Identify the blood parasite species.
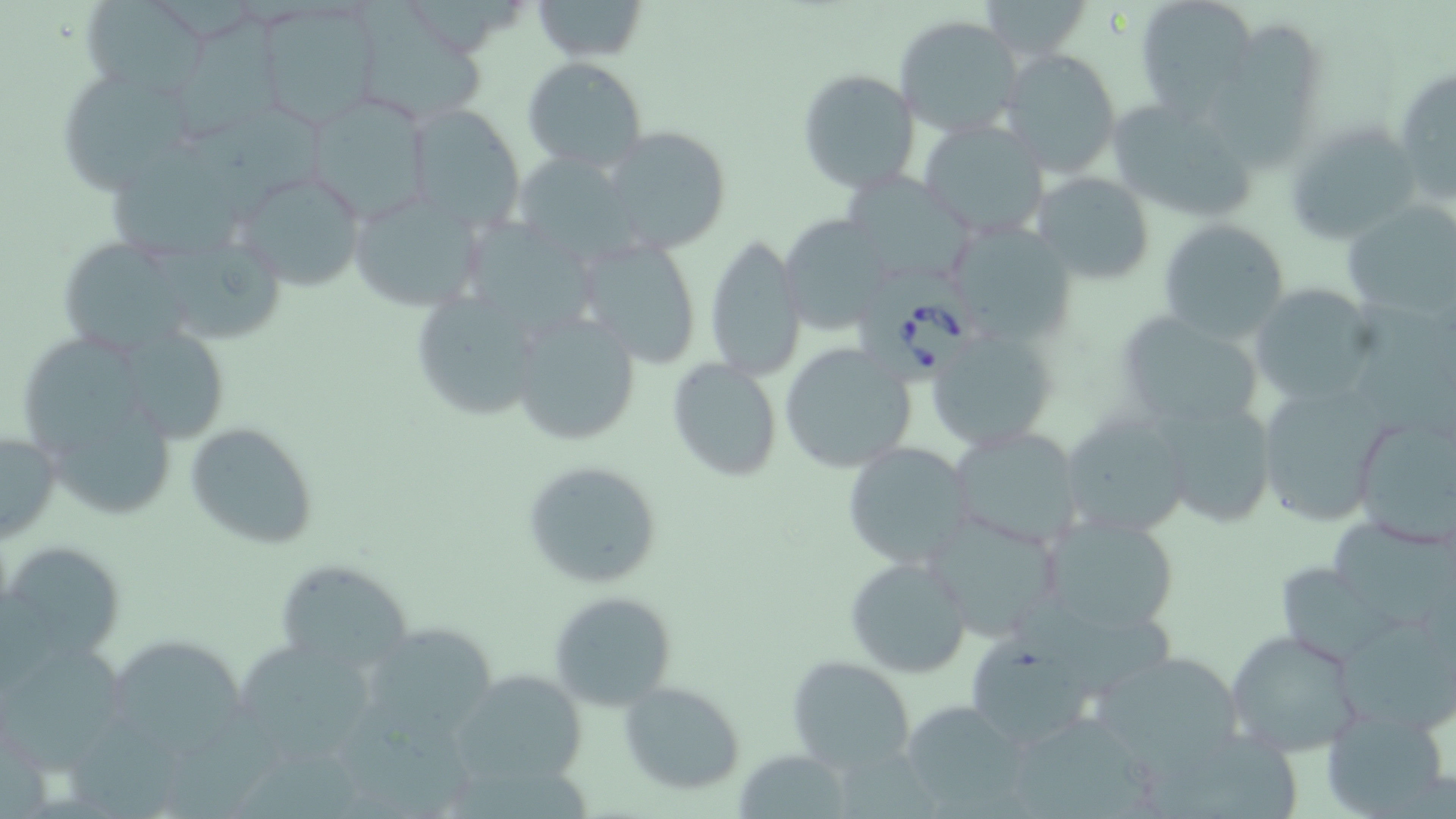

Babesia divergens.

image_size: 1456×819 pixels
preparation: thin blood smear
modality: optical microscopy
uninfected_red_blood_cell_locations: 'approximate bounding boxes as named x1/y1/x2/y2 corners in pixels: (x1=79, y1=0, x2=213, y2=99), (x1=529, y1=0, x2=649, y2=63), (x1=982, y1=0, x2=1094, y2=62), (x1=1133, y1=0, x2=1257, y2=111), (x1=254, y1=3, x2=381, y2=129), (x1=363, y1=4, x2=483, y2=126), (x1=173, y1=14, x2=291, y2=144), (x1=894, y1=14, x2=1026, y2=137), (x1=999, y1=48, x2=1123, y2=178), (x1=522, y1=56, x2=649, y2=171), (x1=1393, y1=62, x2=1456, y2=208), (x1=53, y1=65, x2=200, y2=193), (x1=796, y1=68, x2=920, y2=194), (x1=300, y1=93, x2=431, y2=222), (x1=1103, y1=93, x2=1261, y2=227), (x1=406, y1=106, x2=523, y2=229), (x1=191, y1=112, x2=325, y2=225), (x1=917, y1=117, x2=1052, y2=240), (x1=1282, y1=119, x2=1426, y2=244), (x1=598, y1=125, x2=733, y2=254), (x1=107, y1=141, x2=253, y2=261), (x1=506, y1=150, x2=646, y2=266), (x1=231, y1=167, x2=368, y2=292), (x1=841, y1=171, x2=978, y2=287), (x1=1032, y1=171, x2=1157, y2=285), (x1=348, y1=189, x2=486, y2=312), (x1=1343, y1=201, x2=1456, y2=317), (x1=779, y1=216, x2=898, y2=331), (x1=1157, y1=219, x2=1290, y2=343), (x1=944, y1=221, x2=1078, y2=348), (x1=467, y1=222, x2=602, y2=350), (x1=575, y1=237, x2=703, y2=368), (x1=704, y1=237, x2=806, y2=380), (x1=63, y1=242, x2=188, y2=356), (x1=149, y1=242, x2=287, y2=348), (x1=1249, y1=286, x2=1380, y2=404), (x1=410, y1=293, x2=543, y2=422), (x1=1115, y1=308, x2=1269, y2=436), (x1=510, y1=311, x2=642, y2=446), (x1=925, y1=327, x2=1060, y2=453), (x1=118, y1=328, x2=230, y2=445), (x1=22, y1=332, x2=150, y2=456), (x1=778, y1=343, x2=918, y2=473), (x1=666, y1=359, x2=782, y2=482), (x1=1250, y1=377, x2=1398, y2=530), (x1=1153, y1=393, x2=1282, y2=526), (x1=1348, y1=408, x2=1456, y2=551), (x1=44, y1=410, x2=175, y2=520), (x1=1061, y1=410, x2=1194, y2=538), (x1=185, y1=421, x2=318, y2=549), (x1=947, y1=427, x2=1085, y2=550), (x1=0, y1=428, x2=61, y2=544), (x1=842, y1=441, x2=974, y2=569), (x1=520, y1=458, x2=665, y2=591), (x1=921, y1=510, x2=1065, y2=642), (x1=1036, y1=512, x2=1180, y2=639), (x1=1325, y1=520, x2=1456, y2=625), (x1=6, y1=542, x2=126, y2=663), (x1=845, y1=555, x2=972, y2=678), (x1=275, y1=559, x2=416, y2=673), (x1=1282, y1=567, x2=1402, y2=660), (x1=547, y1=591, x2=677, y2=710), (x1=1012, y1=595, x2=1176, y2=693), (x1=357, y1=618, x2=496, y2=740), (x1=1343, y1=624, x2=1456, y2=732), (x1=1225, y1=629, x2=1364, y2=756), (x1=110, y1=635, x2=247, y2=758), (x1=964, y1=635, x2=1101, y2=748), (x1=243, y1=641, x2=374, y2=763), (x1=3, y1=644, x2=128, y2=767), (x1=1089, y1=648, x2=1249, y2=772), (x1=787, y1=653, x2=915, y2=770), (x1=448, y1=669, x2=591, y2=786), (x1=620, y1=681, x2=745, y2=793), (x1=343, y1=700, x2=472, y2=819), (x1=898, y1=700, x2=1033, y2=815), (x1=1323, y1=708, x2=1451, y2=816), (x1=164, y1=709, x2=289, y2=819), (x1=1016, y1=714, x2=1152, y2=819), (x1=72, y1=715, x2=178, y2=819), (x1=1153, y1=732, x2=1304, y2=819), (x1=240, y1=747, x2=364, y2=819), (x1=738, y1=748, x2=851, y2=818)'
field_of_view: one of a larger specimen
magnification: 1000x
stain: May-Grünwald-Giemsa
babesia_divergens_infected_red_blood_cell_locations: 'approximate bounding boxes as named x1/y1/x2/y2 corners in pixels: (x1=861, y1=270, x2=980, y2=388)'